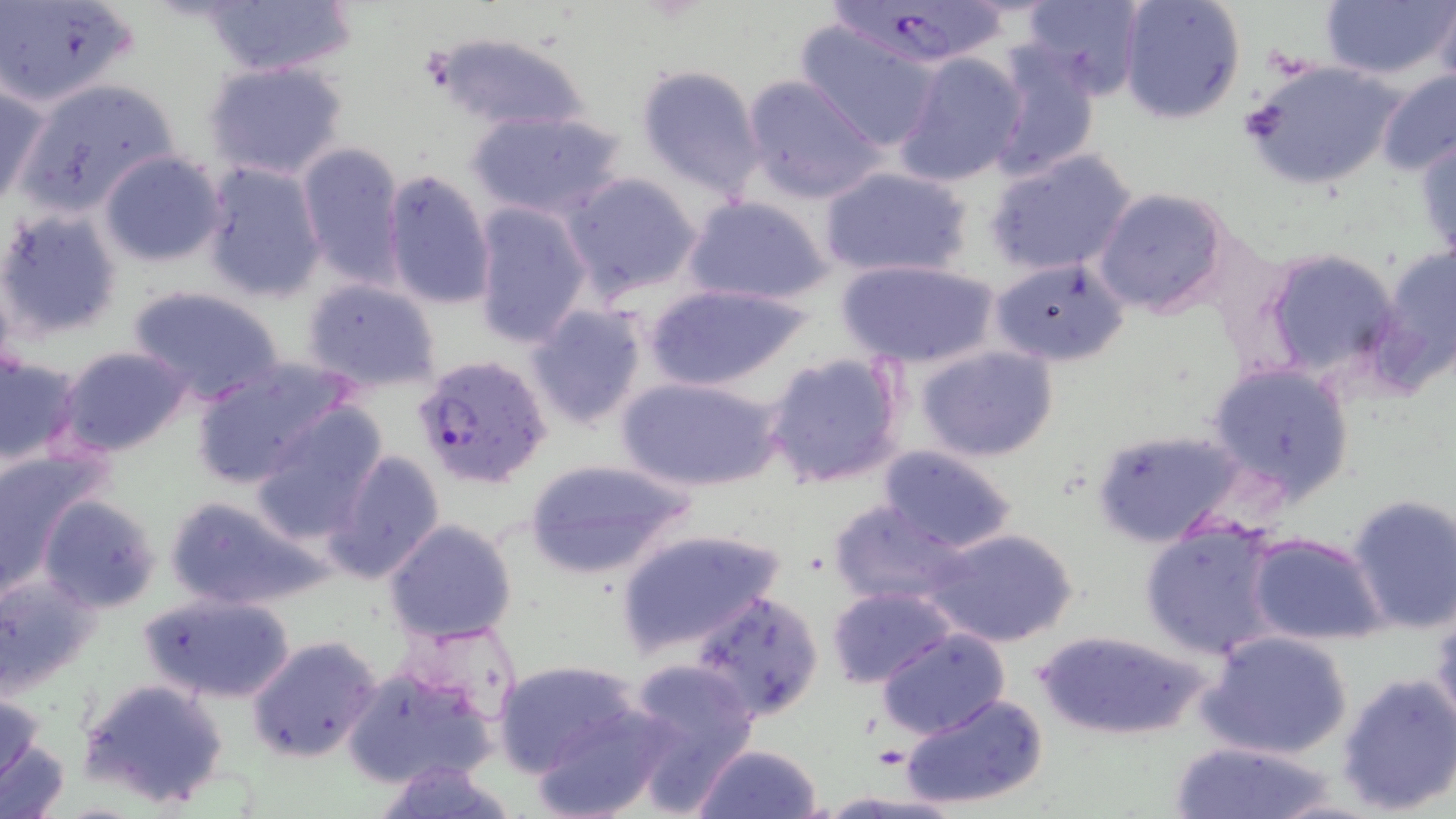
Summary:
  - Coordinate format: approximate bounding boxes as named x1/y1/x2/y2 corners in pixels
  - Uninfected red blood cell locations: (x1=0, y1=0, x2=140, y2=107), (x1=199, y1=0, x2=358, y2=77), (x1=1021, y1=0, x2=1147, y2=100), (x1=1119, y1=0, x2=1246, y2=126), (x1=1319, y1=0, x2=1453, y2=84), (x1=1432, y1=4, x2=1456, y2=88), (x1=795, y1=19, x2=944, y2=152), (x1=434, y1=30, x2=590, y2=135), (x1=985, y1=43, x2=1102, y2=182), (x1=893, y1=50, x2=1029, y2=188), (x1=1244, y1=59, x2=1403, y2=192), (x1=202, y1=60, x2=350, y2=182), (x1=634, y1=64, x2=767, y2=196), (x1=1377, y1=69, x2=1456, y2=178), (x1=742, y1=75, x2=886, y2=202), (x1=16, y1=79, x2=179, y2=217), (x1=0, y1=82, x2=49, y2=209), (x1=465, y1=107, x2=627, y2=219), (x1=1415, y1=132, x2=1456, y2=268), (x1=295, y1=141, x2=406, y2=290), (x1=984, y1=149, x2=1138, y2=276), (x1=100, y1=150, x2=227, y2=268), (x1=199, y1=160, x2=327, y2=304), (x1=818, y1=164, x2=975, y2=279), (x1=380, y1=167, x2=497, y2=311), (x1=559, y1=171, x2=705, y2=302), (x1=1092, y1=186, x2=1234, y2=317), (x1=681, y1=195, x2=832, y2=308), (x1=470, y1=201, x2=594, y2=350), (x1=0, y1=208, x2=122, y2=340), (x1=1259, y1=246, x2=1403, y2=381), (x1=1376, y1=246, x2=1456, y2=386), (x1=989, y1=255, x2=1131, y2=367), (x1=836, y1=257, x2=1000, y2=371), (x1=300, y1=278, x2=445, y2=393), (x1=641, y1=284, x2=814, y2=393), (x1=128, y1=285, x2=286, y2=405), (x1=525, y1=302, x2=653, y2=431), (x1=913, y1=343, x2=1061, y2=463), (x1=58, y1=346, x2=191, y2=458), (x1=762, y1=349, x2=909, y2=490), (x1=0, y1=353, x2=81, y2=467), (x1=188, y1=358, x2=355, y2=491), (x1=1206, y1=360, x2=1355, y2=501), (x1=615, y1=375, x2=784, y2=493), (x1=250, y1=404, x2=388, y2=538), (x1=1092, y1=427, x2=1244, y2=548), (x1=877, y1=445, x2=1018, y2=554), (x1=326, y1=449, x2=446, y2=584), (x1=0, y1=456, x2=89, y2=597), (x1=522, y1=457, x2=694, y2=581), (x1=162, y1=492, x2=326, y2=611), (x1=1345, y1=493, x2=1456, y2=635), (x1=38, y1=494, x2=162, y2=613), (x1=827, y1=498, x2=973, y2=609), (x1=383, y1=519, x2=517, y2=645), (x1=1137, y1=519, x2=1286, y2=662), (x1=612, y1=526, x2=787, y2=659), (x1=923, y1=526, x2=1081, y2=648), (x1=1246, y1=531, x2=1390, y2=645), (x1=0, y1=575, x2=95, y2=700), (x1=828, y1=586, x2=956, y2=689), (x1=689, y1=589, x2=825, y2=721), (x1=139, y1=592, x2=296, y2=705), (x1=399, y1=618, x2=525, y2=723), (x1=875, y1=628, x2=1012, y2=740), (x1=1198, y1=628, x2=1355, y2=760), (x1=1031, y1=629, x2=1214, y2=742), (x1=247, y1=635, x2=382, y2=763), (x1=621, y1=656, x2=761, y2=812), (x1=492, y1=658, x2=643, y2=778), (x1=337, y1=663, x2=497, y2=793), (x1=1334, y1=672, x2=1456, y2=816), (x1=80, y1=676, x2=231, y2=810), (x1=0, y1=691, x2=49, y2=794), (x1=900, y1=691, x2=1049, y2=811), (x1=528, y1=703, x2=673, y2=819), (x1=0, y1=738, x2=70, y2=818), (x1=1167, y1=739, x2=1340, y2=819), (x1=692, y1=743, x2=824, y2=819), (x1=371, y1=761, x2=523, y2=818)
  - Plasmodium falciparum-infected red blood cell locations: (x1=820, y1=0, x2=1022, y2=70), (x1=415, y1=352, x2=553, y2=489)
  - Slide-level diagnosis: Plasmodium falciparum
  - Image size: 1456×819 pixels
  - Modality: light microscopy
  - Preparation: thin blood smear
  - Field of view: one of a larger specimen
  - Magnification: 1000x
  - Stain: May-Grünwald-Giemsa